Assess this cell for malaria.
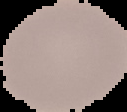

It is uninfected.

image type = segmented cell region with the area outside set to black
image size = 127×112 pixels
preparation = thin blood film